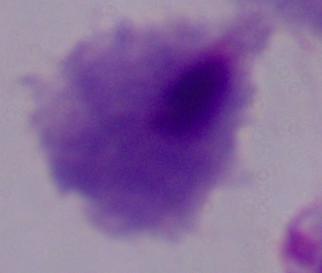 Captured at 1000x magnification. A trichomonad is shown. Photomicrograph.